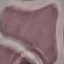

Summary:
  - Result: negative for malaria parasites
  - Capture: smartphone camera at the microscope eyepiece
  - Image type: automatically extracted cell patch, resized to 64 × 64 pixels
  - Preparation: thin blood smear
  - Stain: Giemsa